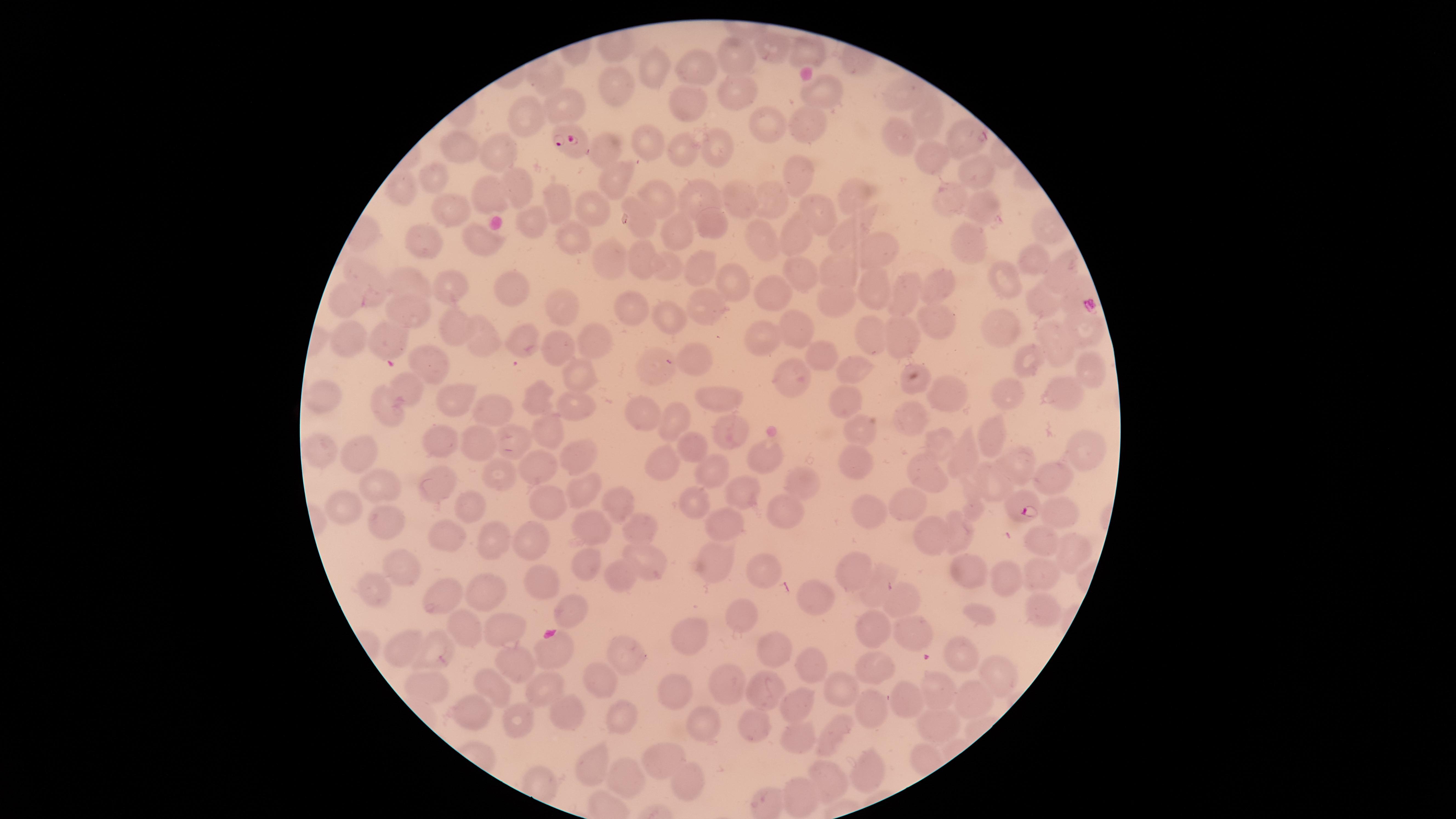

uninfected red blood cells = approximate marker points as (x, y) in pixels: (772, 48), (807, 50), (738, 58), (653, 63), (691, 67), (547, 77), (616, 85), (900, 88), (823, 91), (733, 92), (567, 101), (689, 102), (532, 115), (923, 116), (765, 120), (803, 120), (896, 134), (960, 136), (647, 140), (716, 143), (685, 150), (497, 151), (458, 152), (933, 153), (609, 154), (798, 170), (973, 171), (616, 179), (433, 180), (403, 185), (513, 185), (851, 189), (552, 194), (699, 195), (494, 196), (662, 199), (774, 199), (744, 200), (948, 202), (983, 206), (459, 209), (588, 209), (817, 213), (1047, 219), (715, 220), (531, 221), (638, 224), (682, 233), (844, 233), (478, 236), (576, 236), (795, 236), (762, 240), (974, 246), (424, 248), (876, 248), (1031, 257), (642, 258), (612, 260), (668, 263), (1062, 264), (798, 266), (839, 268), (703, 272), (1004, 277), (369, 281), (941, 285), (408, 286), (733, 287), (518, 289), (870, 289), (447, 291), (904, 293), (835, 295), (769, 297), (343, 300), (562, 302), (1044, 302), (410, 308), (629, 309), (665, 313), (714, 316), (939, 322), (792, 325), (456, 326), (1082, 327), (1001, 329), (874, 335), (591, 336), (907, 336), (349, 337), (389, 338), (1054, 339), (483, 340), (765, 341), (527, 345), (560, 349), (822, 354), (1028, 358), (691, 361), (661, 363), (432, 365), (853, 366), (1085, 372), (579, 376), (793, 377), (909, 385), (410, 387), (1063, 390), (1009, 392), (324, 393), (952, 395), (538, 396), (717, 396), (847, 399), (453, 400), (493, 405), (569, 405), (382, 412), (639, 414), (910, 416), (673, 419), (732, 428), (861, 429), (545, 431), (992, 437), (511, 441), (440, 442), (479, 442), (939, 444), (698, 445), (361, 451), (318, 452), (1081, 452), (572, 454), (964, 454), (769, 456), (669, 459), (1020, 464), (853, 466), (542, 469), (495, 471), (713, 472), (926, 472), (1052, 477), (799, 481), (435, 483), (986, 483), (377, 484), (581, 486), (743, 493), (550, 500), (614, 502), (695, 502), (470, 505), (908, 505), (346, 506), (1062, 511), (868, 512), (784, 516), (385, 524), (594, 525), (730, 525), (962, 532), (445, 533), (640, 533), (931, 533), (527, 539), (489, 540), (1045, 545), (1067, 550), (646, 559), (717, 560), (403, 561), (587, 563), (763, 568), (853, 570), (962, 570), (1042, 573), (617, 574), (1005, 579), (541, 580), (876, 587), (376, 590), (484, 591), (439, 596), (907, 599), (823, 600), (1041, 608), (564, 611), (738, 620), (468, 626), (876, 627), (501, 628), (911, 635), (690, 638), (405, 644), (434, 647), (548, 650), (770, 650), (962, 655), (624, 656), (514, 660), (812, 664), (873, 667), (1000, 671), (602, 680), (720, 682), (428, 686), (548, 687), (678, 687), (497, 689), (841, 689), (770, 690), (941, 692), (901, 698), (974, 699), (802, 701), (477, 710), (868, 713), (569, 715), (628, 716), (515, 720), (701, 725), (939, 727), (761, 730), (833, 734), (802, 743), (663, 759), (926, 759), (595, 766), (868, 768), (626, 776), (827, 778), (690, 779), (804, 797)
stain = Giemsa
visible region = circular
field of view = single
image size = 1456×819 pixels
presence = malaria parasites identified
capture = smartphone photograph through the microscope eyepiece
preparation = thin blood film
parasitized red blood cells = approximate marker points as (x, y) in pixels: (569, 142), (1024, 509)
species = Plasmodium falciparum